Name the blood parasite species.
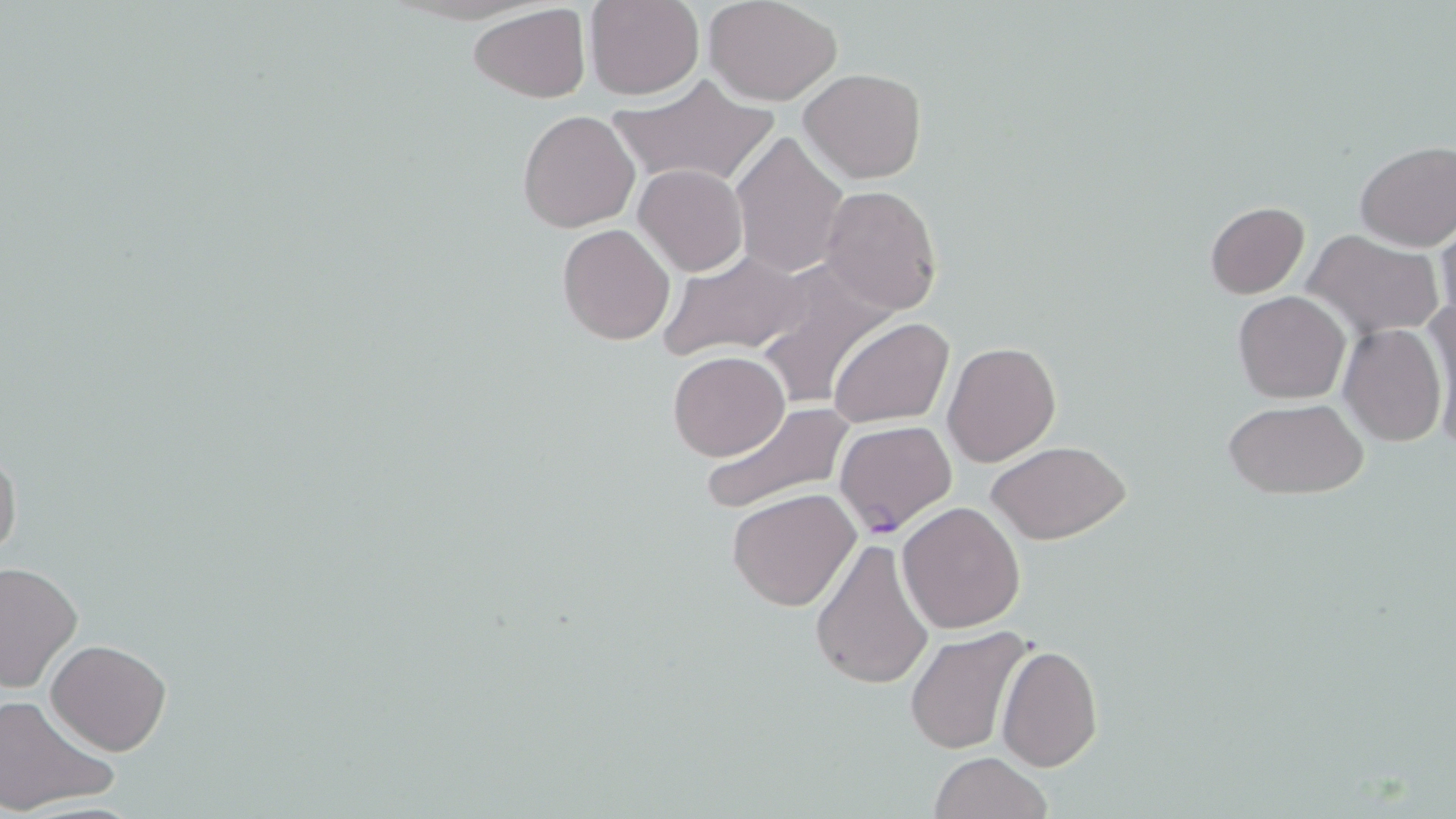

Plasmodium falciparum.

magnification = 1000x
Plasmodium falciparum-infected red blood cell locations = approximate bounding boxes as (x1, y1, x2, y2) in pixels: (835, 419, 957, 537)
field of view = one of a larger specimen
image size = 1456×819 pixels
preparation = thin blood smear
modality = optical microscopy
stain = May-Grünwald-Giemsa
uninfected red blood cell locations = approximate bounding boxes as (x1, y1, x2, y2) in pixels: (585, 0, 703, 100), (705, 0, 843, 105), (468, 3, 590, 103), (799, 68, 928, 184), (608, 76, 780, 191), (516, 109, 639, 232), (730, 134, 849, 279), (1355, 142, 1456, 250), (633, 164, 748, 277), (820, 185, 941, 315), (1203, 201, 1311, 299), (1436, 218, 1456, 331), (557, 223, 675, 346), (1304, 230, 1445, 340), (659, 250, 815, 361), (753, 260, 900, 410), (1233, 291, 1352, 404), (1425, 298, 1456, 447), (829, 317, 954, 428), (1339, 324, 1446, 446), (942, 341, 1062, 467), (667, 351, 790, 461), (1222, 398, 1368, 499), (699, 400, 852, 518), (0, 438, 23, 566), (986, 439, 1132, 545), (727, 488, 861, 611), (898, 500, 1025, 632), (808, 536, 936, 692), (0, 560, 82, 694), (907, 628, 1037, 756), (46, 640, 171, 755), (997, 645, 1103, 771), (0, 693, 117, 817), (928, 752, 1054, 819)